Give the extent of all uninfected red blood cells.
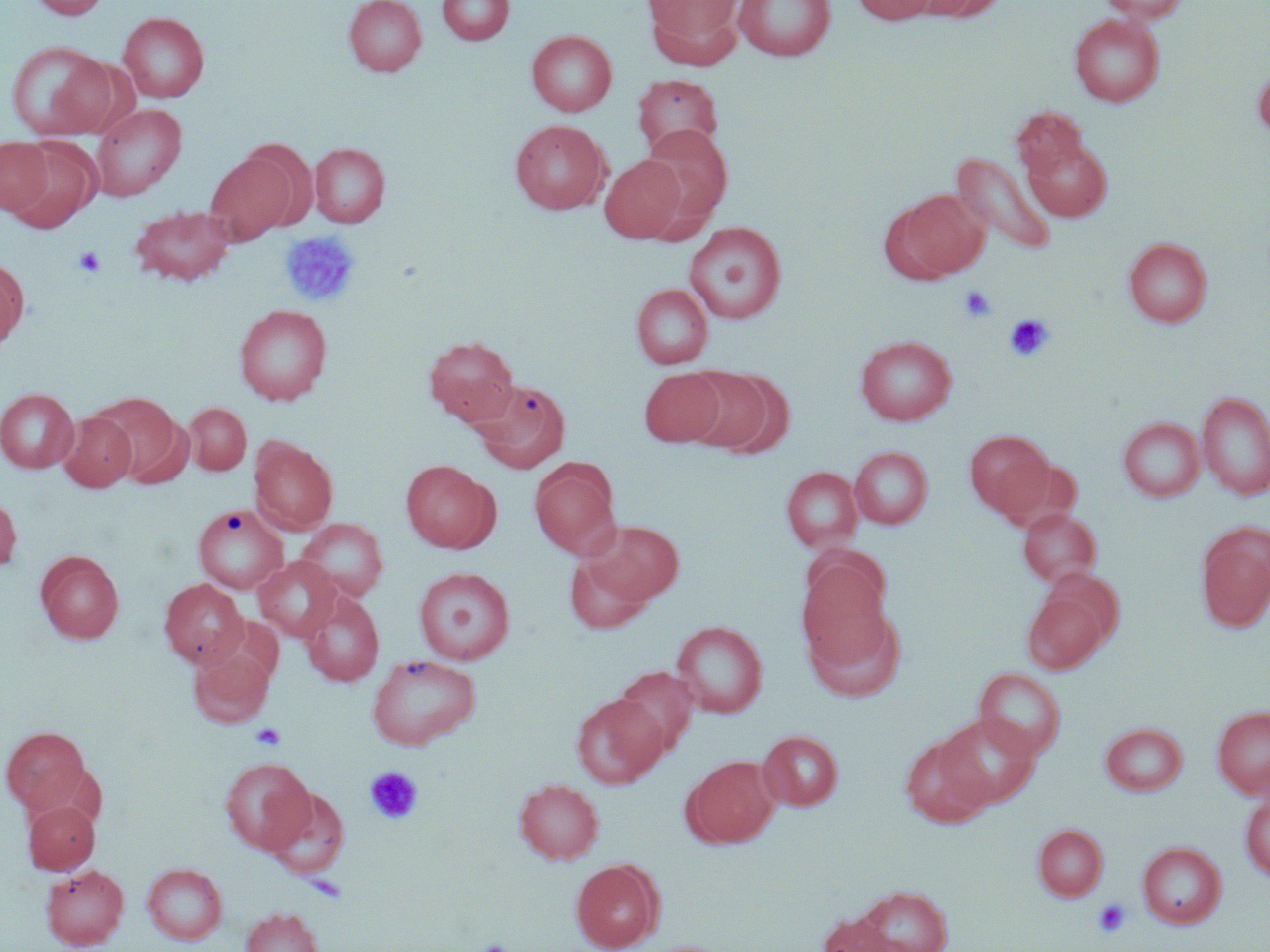

Approximate bounding boxes as (x1, y1, x2, y2) in pixels.
Uninfected red blood cells: (30, 0, 110, 20), (343, 0, 427, 76), (437, 0, 514, 45), (645, 0, 743, 56), (733, 0, 836, 61), (851, 0, 939, 25), (917, 0, 1004, 21), (1098, 0, 1190, 24), (118, 12, 210, 102), (1069, 14, 1165, 107), (526, 30, 617, 116), (5, 40, 113, 140), (1253, 65, 1270, 139), (632, 73, 724, 158), (90, 102, 186, 201), (1011, 106, 1089, 180), (509, 119, 611, 215), (639, 125, 732, 226), (0, 137, 53, 215), (1022, 137, 1112, 222), (5, 138, 101, 232), (241, 140, 318, 231), (309, 142, 390, 227), (950, 151, 1056, 256), (205, 153, 295, 244), (600, 155, 687, 242), (898, 189, 989, 278), (129, 204, 236, 286), (683, 221, 787, 325), (1123, 237, 1212, 327), (0, 257, 29, 352), (631, 284, 713, 368), (233, 304, 332, 404), (423, 335, 519, 425), (855, 335, 956, 424), (680, 367, 779, 455), (639, 369, 725, 447), (469, 378, 571, 473), (0, 388, 79, 473), (1198, 391, 1270, 500), (91, 392, 186, 483), (183, 403, 251, 475), (57, 411, 137, 491), (1118, 417, 1205, 502), (965, 430, 1054, 518), (250, 438, 337, 534), (850, 446, 933, 529), (400, 459, 498, 553), (530, 459, 621, 559), (782, 466, 862, 552), (0, 494, 21, 573), (193, 504, 288, 594), (1018, 507, 1102, 588), (297, 518, 388, 602), (582, 519, 684, 607), (1196, 523, 1270, 631), (35, 550, 124, 643), (564, 551, 656, 634), (798, 553, 892, 663), (253, 556, 342, 641), (414, 567, 515, 665), (159, 578, 248, 668), (1023, 587, 1113, 674), (298, 590, 384, 687), (804, 607, 905, 703), (671, 620, 767, 718), (189, 647, 274, 728), (366, 653, 481, 750), (613, 666, 700, 756), (974, 667, 1067, 760), (571, 693, 668, 788), (1213, 706, 1270, 797), (936, 713, 1041, 809), (1101, 723, 1188, 796), (1, 726, 91, 813), (758, 731, 843, 810), (900, 734, 992, 828), (684, 755, 781, 848), (219, 757, 316, 854), (514, 779, 604, 864), (263, 786, 350, 879), (1240, 790, 1270, 882), (23, 800, 100, 874), (1033, 824, 1108, 902), (1138, 842, 1226, 929), (571, 859, 663, 951), (142, 863, 227, 944), (40, 864, 129, 949), (852, 885, 954, 952), (240, 907, 324, 952), (817, 912, 903, 952).

Platelet locations: (280, 231, 360, 307), (73, 246, 106, 278), (959, 285, 996, 322), (1003, 313, 1054, 362), (250, 723, 287, 750), (364, 766, 423, 825), (1092, 898, 1132, 938), (475, 939, 513, 952). Slide-level diagnosis: negative for blood parasites. May-Grünwald-Giemsa stain. Image is 1270×952 pixels. Optical microscopy. Single field of view. Thin blood film. Captured at 1000x magnification.